Locate and identify every blood parasite.
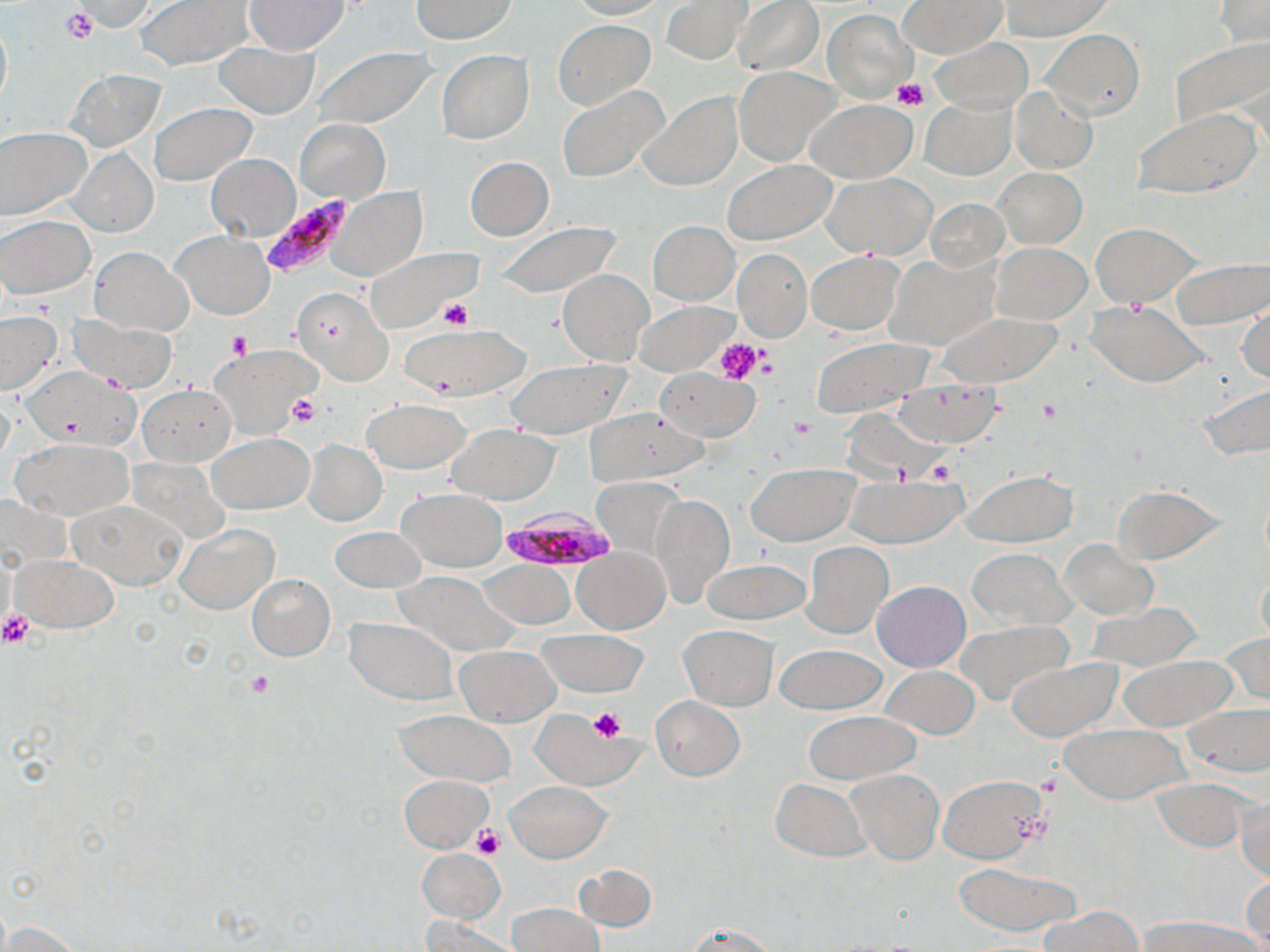
Approximate bounding boxes as named x1/y1/x2/y2 corners in pixels.
Plasmodium falciparum-infected red blood cells: (x1=258, y1=196, x2=352, y2=275), (x1=503, y1=505, x2=618, y2=573).
No Plasmodium ovale, Plasmodium malariae, Plasmodium vivax, Babesia divergens, or Trypanosoma brucei observed.

Uninfected red blood cell locations: (x1=135, y1=0, x2=251, y2=69), (x1=245, y1=0, x2=350, y2=53), (x1=408, y1=0, x2=518, y2=43), (x1=565, y1=0, x2=667, y2=21), (x1=661, y1=0, x2=750, y2=65), (x1=732, y1=0, x2=824, y2=75), (x1=1001, y1=0, x2=1112, y2=40), (x1=70, y1=1, x2=161, y2=34), (x1=901, y1=1, x2=1004, y2=57), (x1=1213, y1=1, x2=1269, y2=48), (x1=822, y1=8, x2=915, y2=103), (x1=0, y1=14, x2=12, y2=110), (x1=553, y1=19, x2=656, y2=110), (x1=1038, y1=29, x2=1144, y2=120), (x1=1169, y1=36, x2=1269, y2=131), (x1=929, y1=37, x2=1032, y2=115), (x1=214, y1=41, x2=319, y2=119), (x1=304, y1=47, x2=436, y2=130), (x1=436, y1=51, x2=534, y2=143), (x1=734, y1=66, x2=840, y2=165), (x1=67, y1=69, x2=163, y2=149), (x1=557, y1=85, x2=670, y2=184), (x1=1010, y1=86, x2=1097, y2=174), (x1=638, y1=92, x2=742, y2=190), (x1=921, y1=97, x2=1016, y2=179), (x1=806, y1=98, x2=917, y2=184), (x1=151, y1=102, x2=256, y2=185), (x1=1133, y1=109, x2=1259, y2=198), (x1=295, y1=119, x2=389, y2=203), (x1=0, y1=127, x2=90, y2=222), (x1=69, y1=147, x2=157, y2=236), (x1=206, y1=152, x2=301, y2=241), (x1=465, y1=155, x2=554, y2=241), (x1=724, y1=159, x2=837, y2=245), (x1=993, y1=167, x2=1087, y2=247), (x1=823, y1=173, x2=936, y2=259), (x1=328, y1=186, x2=426, y2=283), (x1=926, y1=198, x2=1009, y2=272), (x1=1, y1=215, x2=94, y2=298), (x1=648, y1=220, x2=739, y2=305), (x1=492, y1=221, x2=623, y2=297), (x1=1090, y1=223, x2=1199, y2=307), (x1=173, y1=231, x2=272, y2=319), (x1=992, y1=242, x2=1091, y2=323), (x1=362, y1=246, x2=480, y2=333), (x1=89, y1=247, x2=191, y2=334), (x1=733, y1=247, x2=811, y2=341), (x1=807, y1=250, x2=903, y2=334), (x1=888, y1=252, x2=999, y2=350), (x1=1168, y1=256, x2=1269, y2=328), (x1=557, y1=269, x2=654, y2=363), (x1=291, y1=286, x2=394, y2=386), (x1=633, y1=300, x2=734, y2=376), (x1=1087, y1=300, x2=1207, y2=386), (x1=1237, y1=301, x2=1269, y2=386), (x1=0, y1=312, x2=63, y2=396), (x1=935, y1=312, x2=1065, y2=386), (x1=66, y1=314, x2=175, y2=391), (x1=403, y1=325, x2=528, y2=397), (x1=810, y1=338, x2=934, y2=416), (x1=212, y1=344, x2=318, y2=439), (x1=504, y1=358, x2=630, y2=438), (x1=654, y1=368, x2=760, y2=442), (x1=896, y1=379, x2=999, y2=446), (x1=1197, y1=382, x2=1270, y2=460), (x1=137, y1=384, x2=236, y2=467), (x1=363, y1=400, x2=469, y2=474), (x1=581, y1=407, x2=708, y2=484), (x1=448, y1=425, x2=558, y2=505), (x1=208, y1=433, x2=312, y2=513), (x1=12, y1=437, x2=134, y2=520), (x1=302, y1=439, x2=387, y2=525), (x1=746, y1=463, x2=858, y2=545), (x1=962, y1=470, x2=1077, y2=546), (x1=849, y1=475, x2=965, y2=548), (x1=593, y1=477, x2=687, y2=564), (x1=1111, y1=484, x2=1225, y2=564), (x1=398, y1=488, x2=506, y2=571), (x1=650, y1=494, x2=734, y2=606), (x1=70, y1=497, x2=188, y2=590), (x1=176, y1=524, x2=279, y2=614), (x1=331, y1=526, x2=427, y2=593), (x1=1058, y1=538, x2=1158, y2=620), (x1=801, y1=541, x2=892, y2=638), (x1=573, y1=547, x2=669, y2=633), (x1=967, y1=547, x2=1074, y2=629), (x1=13, y1=555, x2=119, y2=632), (x1=700, y1=558, x2=810, y2=625), (x1=483, y1=561, x2=575, y2=628), (x1=393, y1=571, x2=518, y2=656), (x1=1257, y1=571, x2=1270, y2=652), (x1=247, y1=574, x2=335, y2=661), (x1=872, y1=581, x2=970, y2=671), (x1=1088, y1=603, x2=1203, y2=671), (x1=345, y1=619, x2=457, y2=704), (x1=953, y1=621, x2=1071, y2=707), (x1=680, y1=626, x2=779, y2=709), (x1=537, y1=629, x2=648, y2=696), (x1=1218, y1=632, x2=1270, y2=706), (x1=775, y1=644, x2=886, y2=715), (x1=455, y1=645, x2=560, y2=726), (x1=1118, y1=654, x2=1238, y2=730), (x1=1007, y1=658, x2=1120, y2=739), (x1=881, y1=665, x2=979, y2=737), (x1=651, y1=696, x2=744, y2=781), (x1=1184, y1=706, x2=1270, y2=774), (x1=532, y1=709, x2=634, y2=787), (x1=396, y1=710, x2=515, y2=786), (x1=805, y1=710, x2=920, y2=784), (x1=1060, y1=723, x2=1191, y2=802), (x1=847, y1=768, x2=943, y2=864), (x1=399, y1=774, x2=491, y2=853), (x1=937, y1=774, x2=1047, y2=863), (x1=1150, y1=777, x2=1256, y2=853), (x1=771, y1=778, x2=871, y2=861), (x1=507, y1=781, x2=611, y2=862), (x1=1236, y1=792, x2=1269, y2=885), (x1=417, y1=849, x2=504, y2=922), (x1=952, y1=862, x2=1082, y2=937), (x1=574, y1=864, x2=657, y2=932), (x1=1241, y1=874, x2=1270, y2=947), (x1=506, y1=902, x2=604, y2=951), (x1=1038, y1=905, x2=1141, y2=952), (x1=1133, y1=916, x2=1263, y2=951), (x1=420, y1=918, x2=523, y2=952), (x1=2, y1=920, x2=84, y2=951), (x1=686, y1=922, x2=782, y2=950). Platelet locations: (x1=59, y1=6, x2=97, y2=45), (x1=892, y1=78, x2=928, y2=112), (x1=440, y1=298, x2=473, y2=329), (x1=226, y1=330, x2=251, y2=359), (x1=714, y1=339, x2=765, y2=385), (x1=286, y1=393, x2=321, y2=427), (x1=1035, y1=397, x2=1064, y2=425), (x1=786, y1=415, x2=816, y2=439), (x1=924, y1=459, x2=956, y2=482), (x1=0, y1=610, x2=36, y2=648), (x1=248, y1=670, x2=276, y2=698), (x1=588, y1=707, x2=626, y2=742), (x1=472, y1=825, x2=505, y2=860). Slide-level diagnosis: Plasmodium falciparum. Thin blood smear. Image is 1270×952 pixels. 1000x magnification. May-Grünwald-Giemsa-stained preparation. One field of a larger specimen. Optical microscopy.